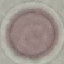
Summary:
  - Result: no malaria parasites seen
  - Image type: automatically extracted cell patch, resized to 64 × 64 pixels
  - Capture: smartphone through the microscope eyepiece
  - Preparation: thin smear
  - Stain: Giemsa